Locate and identify every blood parasite.
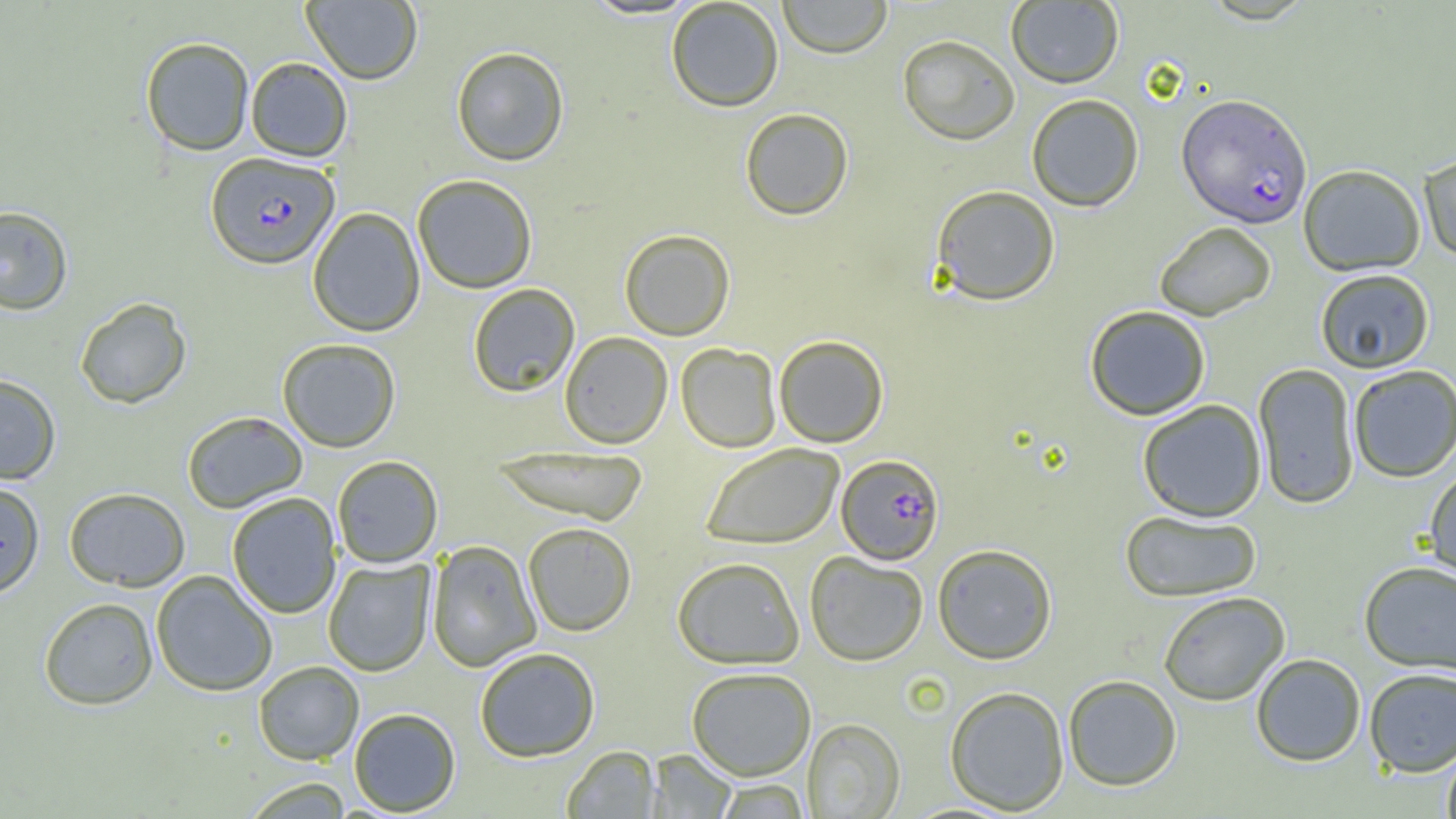

Approximate bounding boxes as named x1/y1/x2/y2 corners in pixels.
Plasmodium falciparum-infected red blood cells: (x1=1177, y1=93, x2=1312, y2=228), (x1=205, y1=151, x2=340, y2=269), (x1=836, y1=454, x2=944, y2=565).
No Plasmodium ovale, Plasmodium malariae, Plasmodium vivax, Babesia divergens, or Trypanosoma brucei observed.

Summary:
  - Uninfected red blood cell locations: (x1=301, y1=0, x2=423, y2=85), (x1=666, y1=0, x2=784, y2=112), (x1=777, y1=0, x2=893, y2=58), (x1=1006, y1=1, x2=1124, y2=88), (x1=897, y1=34, x2=1020, y2=145), (x1=140, y1=36, x2=255, y2=156), (x1=451, y1=46, x2=569, y2=166), (x1=245, y1=57, x2=352, y2=162), (x1=1026, y1=93, x2=1144, y2=211), (x1=740, y1=107, x2=854, y2=220), (x1=1419, y1=152, x2=1456, y2=263), (x1=1298, y1=164, x2=1426, y2=276), (x1=412, y1=174, x2=538, y2=294), (x1=930, y1=184, x2=1060, y2=305), (x1=0, y1=205, x2=73, y2=315), (x1=307, y1=207, x2=426, y2=337), (x1=1154, y1=221, x2=1276, y2=321), (x1=619, y1=229, x2=735, y2=340), (x1=1315, y1=268, x2=1435, y2=373), (x1=467, y1=283, x2=580, y2=397), (x1=74, y1=297, x2=192, y2=409), (x1=1084, y1=304, x2=1211, y2=420), (x1=559, y1=331, x2=673, y2=448), (x1=773, y1=335, x2=889, y2=448), (x1=277, y1=338, x2=401, y2=452), (x1=676, y1=343, x2=782, y2=453), (x1=1252, y1=363, x2=1360, y2=509), (x1=1348, y1=365, x2=1456, y2=482), (x1=0, y1=373, x2=61, y2=484), (x1=1137, y1=399, x2=1267, y2=522), (x1=182, y1=411, x2=308, y2=513), (x1=700, y1=443, x2=844, y2=549), (x1=489, y1=446, x2=651, y2=526), (x1=332, y1=455, x2=443, y2=568), (x1=1423, y1=466, x2=1456, y2=582), (x1=0, y1=479, x2=45, y2=599), (x1=63, y1=487, x2=191, y2=591), (x1=226, y1=492, x2=342, y2=619), (x1=1119, y1=509, x2=1263, y2=601), (x1=522, y1=522, x2=637, y2=636), (x1=426, y1=539, x2=542, y2=673), (x1=932, y1=543, x2=1057, y2=664), (x1=805, y1=551, x2=929, y2=666), (x1=671, y1=556, x2=805, y2=669), (x1=322, y1=558, x2=436, y2=676), (x1=1359, y1=561, x2=1456, y2=675), (x1=151, y1=570, x2=278, y2=696), (x1=1157, y1=591, x2=1290, y2=706), (x1=38, y1=596, x2=159, y2=710), (x1=474, y1=647, x2=601, y2=762), (x1=1251, y1=653, x2=1367, y2=766), (x1=253, y1=660, x2=364, y2=765), (x1=686, y1=666, x2=817, y2=781), (x1=1363, y1=667, x2=1456, y2=776), (x1=1063, y1=674, x2=1182, y2=791), (x1=944, y1=685, x2=1070, y2=814), (x1=349, y1=708, x2=461, y2=815), (x1=802, y1=718, x2=905, y2=818), (x1=1441, y1=741, x2=1456, y2=819), (x1=562, y1=746, x2=661, y2=818), (x1=647, y1=749, x2=738, y2=818), (x1=240, y1=776, x2=354, y2=818), (x1=714, y1=779, x2=809, y2=818)
  - Slide-level diagnosis: Plasmodium falciparum
  - Field of view: single
  - Modality: light microscopy
  - Magnification: 1000x
  - Image size: 1456×819 pixels
  - Preparation: thin blood film